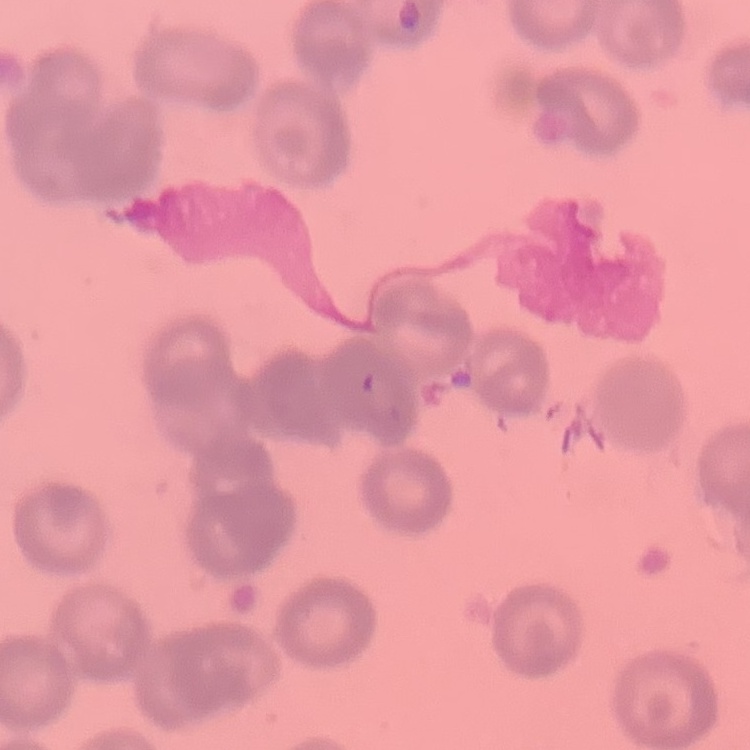

erythrocyte morphology = rouleaux formation
stain = Field's or Giemsa
preparation = thin blood film
image type = square crop of a larger photomicrograph